Describe the morphology of the red blood cells.
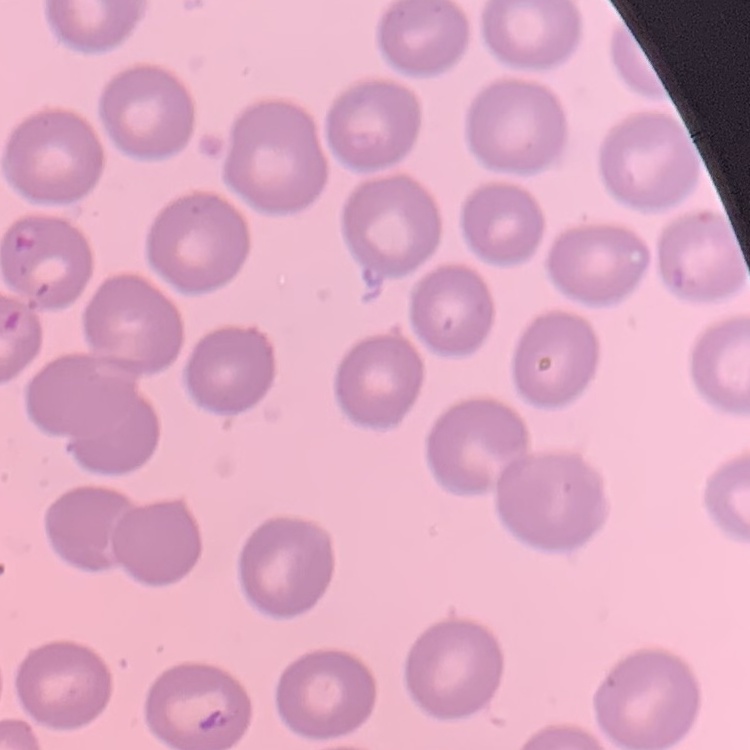

No rouleaux formation.

Thin peripheral smear. Stained with either Field's or Giemsa. Square crop of a larger photomicrograph.